Assess this cell for malaria.
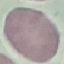
Uninfected.

Giemsa stain. Thin blood smear. Cell patch, automatically extracted from a larger field of view and resized to 64 × 64 pixels. Acquired by smartphone through the microscope eyepiece.